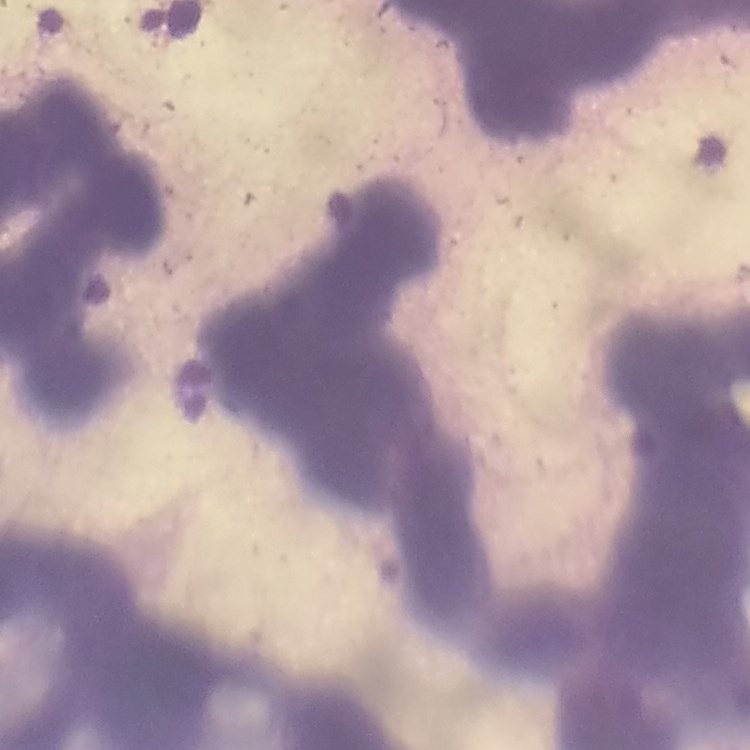
erythrocyte morphology = rouleaux formation
stain = Field's or Giemsa
preparation = thin peripheral smear
image type = one tile cut from a larger photomicrograph